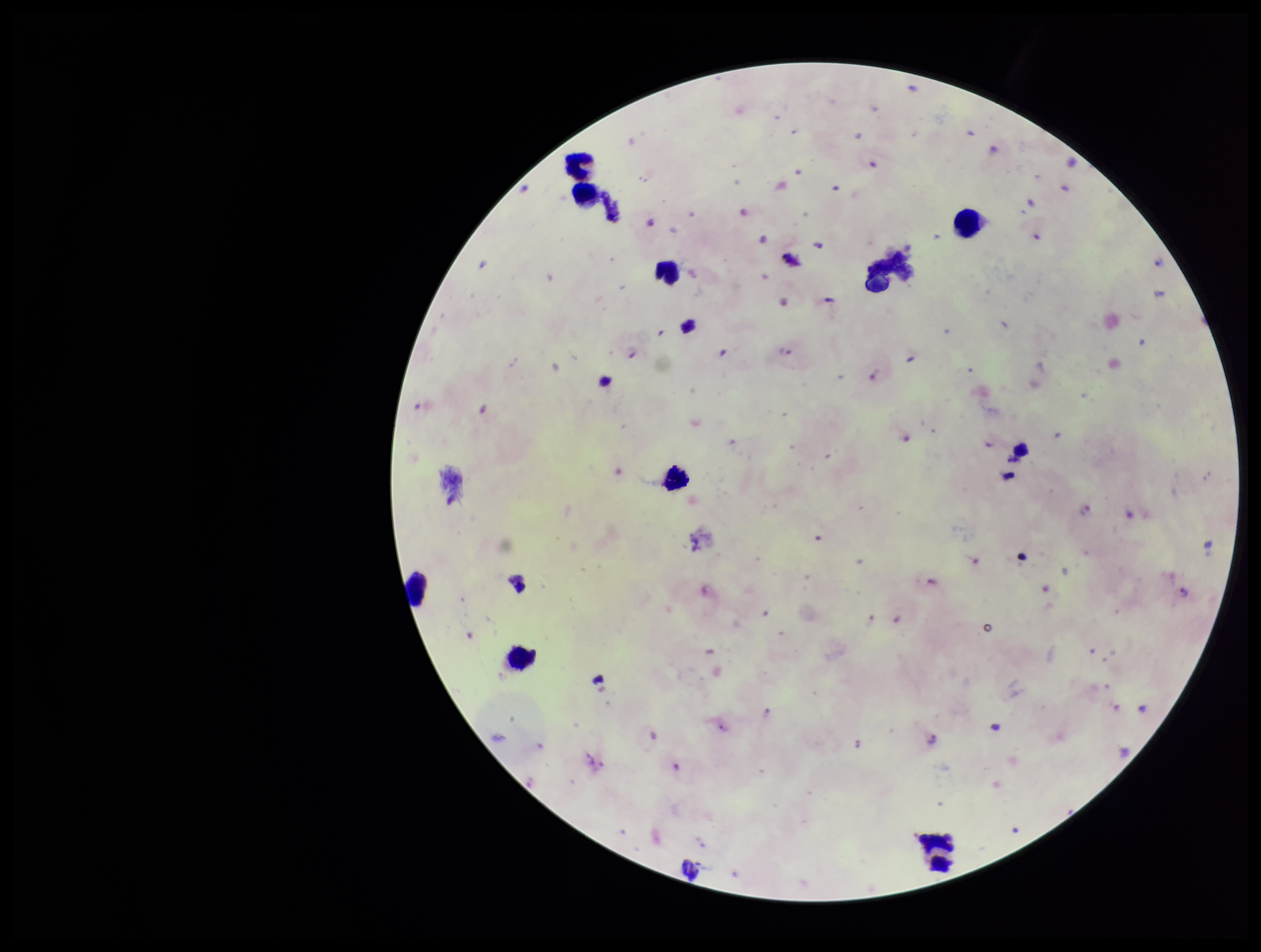

leukocyte count = 9
image size = 1261×952 pixels
parasite count = 24
preparation = thick
Plasmodium parasites = detected
stain = Giemsa
patient malaria status = positive
field of view = one from this slide
species reported for this patient = Plasmodium falciparum
capture = smartphone photograph through the microscope eyepiece